Name the parasite shown.
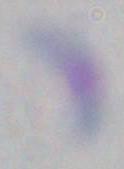
Toxoplasma gondii.

Summary:
  - Modality: photomicrograph
  - Magnification: 1000x